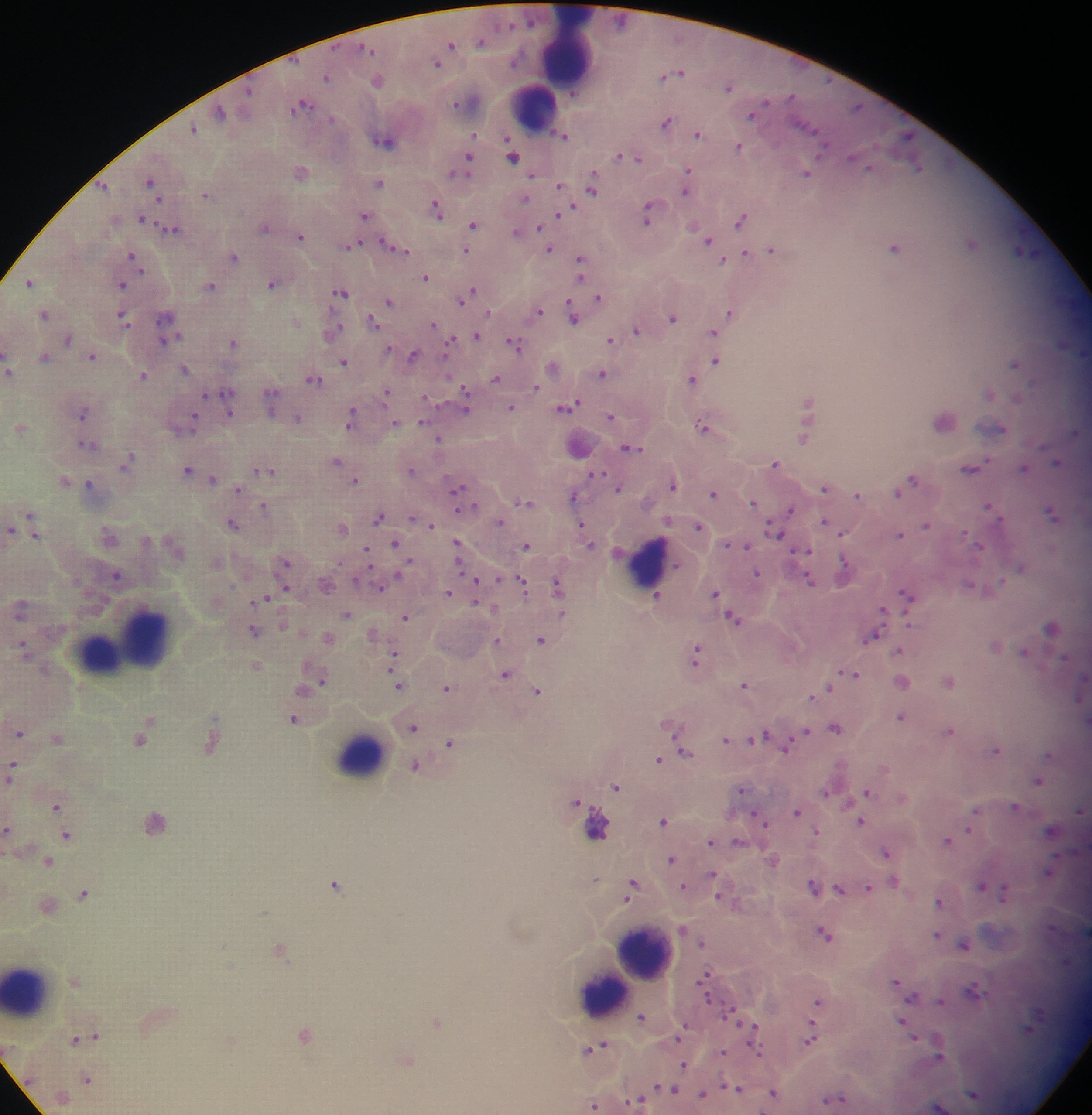
Approximate centers as (x, y) in pixels. Malaria parasite locations: (481, 41), (450, 46), (436, 62), (677, 73), (326, 77), (377, 80), (728, 86), (461, 103), (301, 105), (219, 112), (752, 114), (666, 121), (193, 129), (473, 134), (698, 134), (562, 135), (384, 139), (739, 146), (512, 154), (632, 157), (468, 159), (918, 166), (464, 167), (868, 167), (300, 171), (458, 171), (687, 172), (806, 172), (531, 175), (150, 182), (379, 183), (558, 185), (103, 186), (592, 187), (686, 190), (205, 194), (525, 197), (436, 209), (569, 209), (650, 212), (364, 214), (560, 214), (740, 218), (142, 219), (473, 224), (264, 227), (540, 227), (171, 228), (516, 232), (300, 237), (709, 240), (972, 242), (350, 245), (894, 247), (395, 248), (549, 249), (771, 249), (465, 250), (1022, 251), (745, 253), (132, 255), (233, 256), (730, 259), (723, 261), (580, 266), (425, 277), (29, 281), (272, 283), (121, 284), (209, 285), (340, 292), (470, 293), (598, 298), (463, 299), (389, 301), (538, 311), (731, 312), (43, 314), (573, 315), (122, 316), (672, 316), (373, 321), (167, 322), (432, 324), (637, 330), (331, 331), (712, 332), (166, 335), (475, 335), (66, 338), (611, 340), (233, 341), (449, 342), (515, 344), (389, 349), (412, 354), (92, 356), (43, 357), (716, 359), (344, 361), (1015, 363), (553, 366), (9, 368), (184, 368), (602, 374), (142, 375), (495, 378), (692, 378), (313, 379), (535, 386), (989, 393), (207, 394), (386, 394), (270, 395), (465, 395), (226, 398), (808, 402), (568, 406), (512, 407), (228, 408), (83, 412), (610, 416), (351, 417), (297, 418), (944, 420), (423, 421), (188, 422), (394, 424), (703, 426), (20, 427), (995, 428), (1076, 431), (804, 437), (438, 438), (87, 445), (578, 445), (630, 448), (335, 460), (1056, 462), (775, 463), (126, 464), (1022, 467), (969, 468), (187, 469), (262, 470), (411, 470), (595, 475), (211, 479), (64, 480), (355, 480), (910, 480), (90, 484), (672, 484), (618, 487), (824, 487), (237, 488), (900, 490), (458, 491), (714, 493), (857, 494), (573, 495), (524, 501), (753, 502), (460, 503), (264, 506), (990, 507), (790, 510), (1052, 513), (378, 517), (415, 519), (423, 521), (824, 521), (499, 522), (232, 523), (31, 524), (431, 524), (698, 525), (926, 525), (342, 527), (582, 527), (10, 530), (775, 531), (842, 532), (900, 534), (109, 537), (589, 541), (396, 543), (734, 544), (527, 545), (978, 545), (457, 548), (366, 550), (806, 550), (216, 562), (285, 563), (843, 564), (1021, 567), (757, 573), (116, 575), (809, 578), (475, 581), (1002, 582), (522, 584), (325, 585), (970, 585), (558, 586), (380, 587), (448, 592), (715, 593), (907, 594), (657, 596), (264, 599), (20, 608), (884, 611), (346, 614), (405, 616), (733, 618), (1051, 627), (253, 630), (373, 634), (327, 637), (870, 638), (497, 640), (541, 640), (995, 646), (24, 647), (898, 650), (1025, 651), (394, 654), (697, 655), (256, 665), (851, 673), (505, 674), (948, 680), (320, 681), (902, 681), (398, 684), (745, 684), (447, 687), (828, 688), (304, 689), (537, 691), (821, 692), (813, 696), (1079, 697), (901, 717), (149, 720), (294, 720), (413, 726), (670, 726), (835, 727), (949, 730), (19, 732), (804, 733), (760, 736), (57, 737), (141, 740), (726, 740), (751, 740), (678, 742), (211, 743), (449, 743), (787, 744), (996, 749), (685, 751), (1050, 754), (658, 759), (415, 766), (884, 768), (11, 771), (1038, 780), (616, 786), (741, 789), (866, 791), (826, 792), (577, 803), (56, 805), (1015, 806), (976, 810), (1079, 810), (797, 811), (760, 818), (663, 820), (153, 822), (861, 822), (595, 827), (8, 829), (1051, 830), (970, 831), (816, 832), (66, 834), (948, 839), (711, 842), (737, 842), (886, 852), (671, 858), (772, 859), (47, 861), (1049, 872), (712, 874), (894, 881), (335, 884), (981, 885), (813, 886), (631, 887), (684, 887), (839, 888), (867, 888), (1004, 891), (84, 893), (939, 901), (46, 905), (264, 911), (683, 930), (825, 932), (937, 934), (702, 941), (964, 945), (279, 948), (705, 980), (74, 981), (896, 981), (974, 991), (913, 997), (817, 1001), (941, 1002), (641, 1016), (437, 1022), (904, 1022), (753, 1026), (813, 1029), (1028, 1030), (681, 1032), (95, 1034), (304, 1035), (811, 1037), (914, 1037), (74, 1039), (596, 1047), (938, 1050), (722, 1052), (405, 1058), (684, 1065), (86, 1079), (670, 1087), (736, 1088), (773, 1092), (702, 1094), (973, 1094), (833, 1099), (637, 1102), (595, 1105), (939, 1106). Leukocyte locations: (567, 52), (532, 107), (648, 562), (130, 639), (358, 754), (644, 953), (628, 973), (27, 988), (601, 993). Image is 1092×1115 pixels. Sample from Ghana. Photographed through a microscope with a mobile-phone camera. One field of view. Thick blood film.